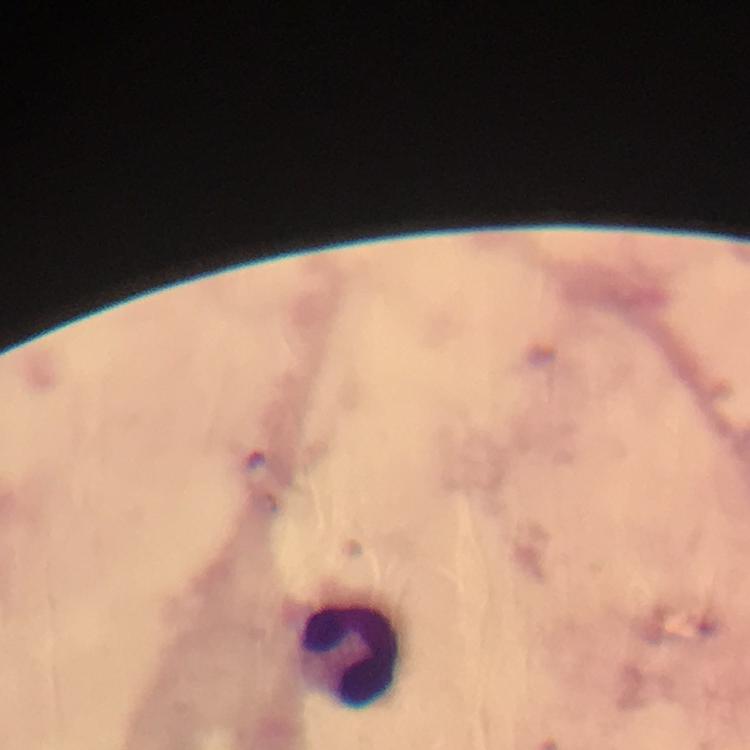
Approximate centers as (x, y) in pixels.
Summary:
  - Leukocyte locations: (349, 651)
  - Capture: smartphone mounted on the microscope
  - Context: from a malaria diagnostic workup
  - Magnification: 100x
  - Immersion oil: used
  - Cropped from: a single field of view
  - Malaria parasites: none detected
  - Image size: 750×750 pixels
  - Stain: Giemsa
  - Preparation: thick blood film